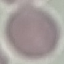
Summary:
  - Malaria status: uninfected
  - Preparation: thin smear
  - Stain: Giemsa
  - Capture: smartphone through the microscope eyepiece
  - Image type: cell patch, automatically extracted from a larger field of view and resized to 64 × 64 pixels